Classify this cell by malaria status.
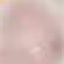

It is uninfected.

Thin blood smear. Automatically extracted cell patch, resized to 64 × 64 pixels. Giemsa stain. Photographed with a smartphone camera at the microscope eyepiece.